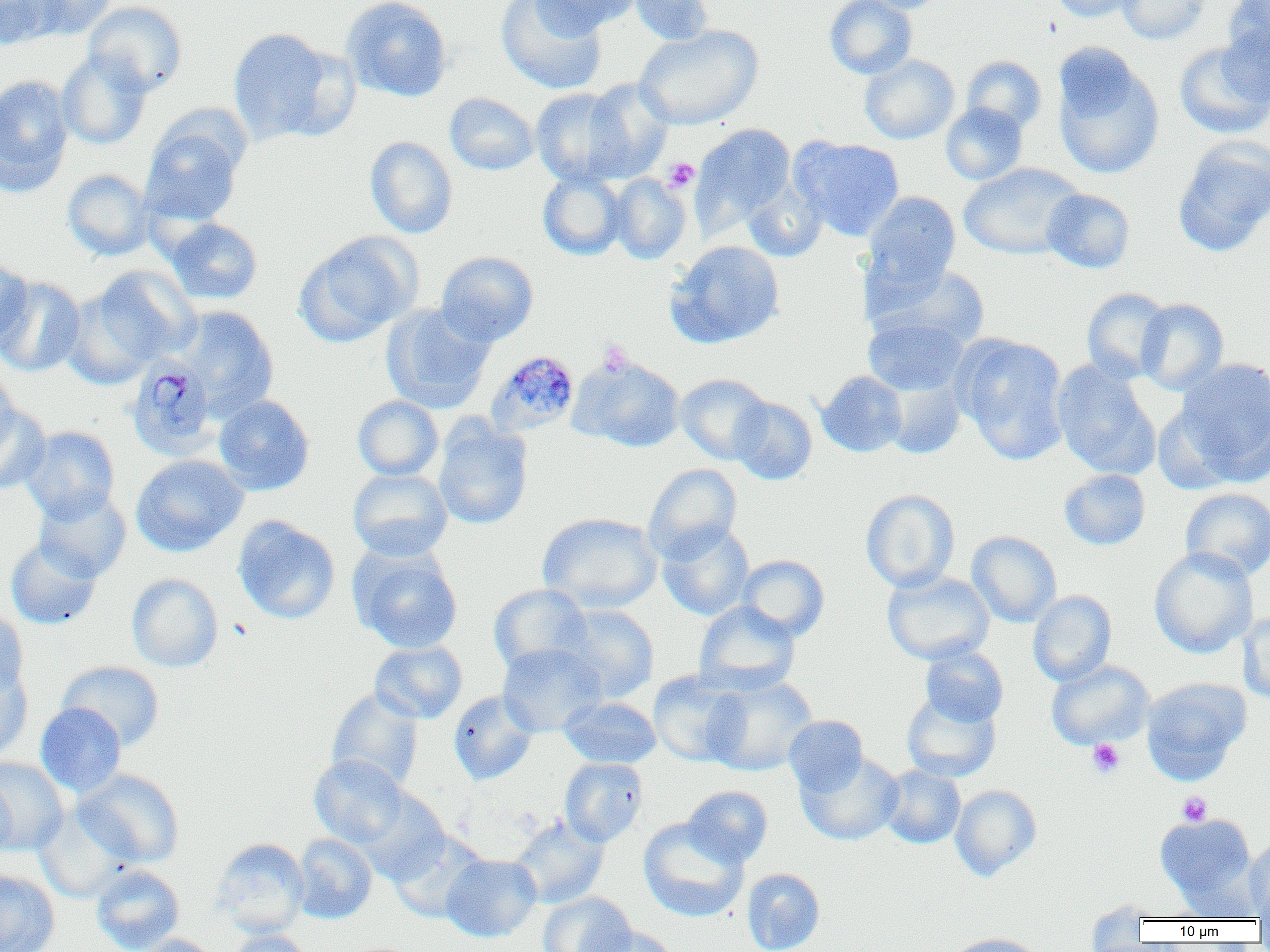
Summary:
  - Coordinate format: approximate bounding boxes as named x1/y1/x2/y2 corners in pixels
  - Uninfected red blood cell locations: (x1=0, y1=0, x2=63, y2=51), (x1=24, y1=0, x2=117, y2=39), (x1=341, y1=0, x2=452, y2=101), (x1=496, y1=0, x2=607, y2=95), (x1=528, y1=0, x2=639, y2=35), (x1=627, y1=0, x2=715, y2=45), (x1=824, y1=0, x2=917, y2=79), (x1=853, y1=0, x2=947, y2=13), (x1=1049, y1=0, x2=1142, y2=22), (x1=1115, y1=0, x2=1211, y2=44), (x1=1224, y1=0, x2=1270, y2=61), (x1=84, y1=1, x2=188, y2=96), (x1=1218, y1=18, x2=1270, y2=107), (x1=634, y1=25, x2=763, y2=130), (x1=227, y1=28, x2=347, y2=144), (x1=1174, y1=41, x2=1270, y2=139), (x1=56, y1=51, x2=152, y2=150), (x1=1051, y1=51, x2=1165, y2=180), (x1=859, y1=54, x2=959, y2=145), (x1=961, y1=56, x2=1047, y2=134), (x1=0, y1=74, x2=73, y2=195), (x1=582, y1=79, x2=674, y2=183), (x1=531, y1=88, x2=629, y2=187), (x1=444, y1=93, x2=538, y2=175), (x1=940, y1=102, x2=1028, y2=185), (x1=141, y1=120, x2=245, y2=227), (x1=691, y1=123, x2=796, y2=232), (x1=1172, y1=135, x2=1270, y2=257), (x1=365, y1=136, x2=458, y2=239), (x1=793, y1=137, x2=905, y2=240), (x1=958, y1=162, x2=1086, y2=260), (x1=62, y1=169, x2=155, y2=260), (x1=538, y1=171, x2=627, y2=259), (x1=609, y1=173, x2=691, y2=264), (x1=742, y1=179, x2=827, y2=262), (x1=1041, y1=188, x2=1135, y2=273), (x1=862, y1=191, x2=960, y2=294), (x1=164, y1=218, x2=262, y2=305), (x1=294, y1=232, x2=422, y2=347), (x1=665, y1=240, x2=785, y2=348), (x1=436, y1=251, x2=538, y2=346), (x1=0, y1=258, x2=32, y2=341), (x1=870, y1=262, x2=992, y2=350), (x1=86, y1=266, x2=200, y2=369), (x1=0, y1=276, x2=85, y2=377), (x1=62, y1=285, x2=163, y2=389), (x1=1081, y1=288, x2=1172, y2=383), (x1=1136, y1=298, x2=1229, y2=395), (x1=381, y1=303, x2=495, y2=412), (x1=174, y1=305, x2=279, y2=417), (x1=863, y1=314, x2=968, y2=396), (x1=956, y1=335, x2=1070, y2=464), (x1=570, y1=355, x2=685, y2=452), (x1=1175, y1=357, x2=1270, y2=485), (x1=1051, y1=360, x2=1160, y2=480), (x1=0, y1=366, x2=20, y2=459), (x1=817, y1=370, x2=908, y2=457), (x1=676, y1=373, x2=773, y2=464), (x1=883, y1=373, x2=966, y2=458), (x1=213, y1=394, x2=314, y2=495), (x1=352, y1=396, x2=443, y2=481), (x1=730, y1=397, x2=817, y2=485), (x1=0, y1=405, x2=50, y2=494), (x1=433, y1=418, x2=533, y2=530), (x1=20, y1=426, x2=120, y2=523), (x1=131, y1=454, x2=248, y2=557), (x1=644, y1=463, x2=742, y2=562), (x1=348, y1=469, x2=453, y2=561), (x1=1058, y1=469, x2=1150, y2=550), (x1=1180, y1=487, x2=1270, y2=581), (x1=34, y1=489, x2=132, y2=581), (x1=860, y1=489, x2=960, y2=592), (x1=537, y1=512, x2=662, y2=613), (x1=232, y1=515, x2=340, y2=624), (x1=657, y1=522, x2=755, y2=620), (x1=967, y1=531, x2=1062, y2=628), (x1=5, y1=537, x2=102, y2=630), (x1=349, y1=544, x2=463, y2=654), (x1=1149, y1=546, x2=1258, y2=658), (x1=736, y1=555, x2=829, y2=641), (x1=882, y1=570, x2=994, y2=665), (x1=126, y1=573, x2=223, y2=672), (x1=488, y1=583, x2=592, y2=674), (x1=1028, y1=590, x2=1117, y2=686), (x1=694, y1=600, x2=800, y2=694), (x1=552, y1=604, x2=660, y2=703), (x1=0, y1=607, x2=29, y2=699), (x1=1239, y1=610, x2=1270, y2=705), (x1=369, y1=640, x2=467, y2=724), (x1=497, y1=642, x2=607, y2=737), (x1=920, y1=646, x2=1008, y2=727), (x1=1046, y1=659, x2=1155, y2=750), (x1=56, y1=661, x2=165, y2=750), (x1=0, y1=662, x2=32, y2=762), (x1=648, y1=670, x2=747, y2=766), (x1=701, y1=675, x2=818, y2=776), (x1=1141, y1=677, x2=1250, y2=782), (x1=327, y1=689, x2=424, y2=791), (x1=448, y1=690, x2=538, y2=785), (x1=901, y1=690, x2=1001, y2=783), (x1=559, y1=696, x2=661, y2=768), (x1=35, y1=702, x2=126, y2=797), (x1=783, y1=715, x2=869, y2=796), (x1=796, y1=751, x2=904, y2=846), (x1=309, y1=754, x2=410, y2=848), (x1=0, y1=757, x2=70, y2=855), (x1=560, y1=758, x2=648, y2=846), (x1=878, y1=766, x2=965, y2=849), (x1=74, y1=769, x2=185, y2=867), (x1=0, y1=777, x2=17, y2=861), (x1=950, y1=784, x2=1042, y2=881), (x1=683, y1=786, x2=773, y2=868), (x1=353, y1=787, x2=451, y2=884), (x1=33, y1=804, x2=134, y2=902), (x1=1154, y1=813, x2=1259, y2=908), (x1=509, y1=815, x2=610, y2=909), (x1=638, y1=817, x2=748, y2=922), (x1=388, y1=830, x2=490, y2=924), (x1=292, y1=833, x2=377, y2=924), (x1=1244, y1=836, x2=1270, y2=919), (x1=212, y1=838, x2=310, y2=938), (x1=440, y1=854, x2=542, y2=942), (x1=91, y1=864, x2=185, y2=952), (x1=742, y1=867, x2=825, y2=952), (x1=0, y1=869, x2=60, y2=952), (x1=538, y1=892, x2=637, y2=952), (x1=1084, y1=899, x2=1167, y2=943), (x1=588, y1=925, x2=680, y2=952), (x1=226, y1=929, x2=313, y2=952), (x1=943, y1=933, x2=1047, y2=952), (x1=132, y1=934, x2=223, y2=952)
  - Plasmodium malariae-infected red blood cell locations: (x1=485, y1=350, x2=580, y2=438), (x1=131, y1=357, x2=222, y2=461)
  - Platelet locations: (x1=662, y1=157, x2=699, y2=193), (x1=597, y1=340, x2=633, y2=376), (x1=1087, y1=739, x2=1125, y2=779), (x1=1177, y1=792, x2=1211, y2=826)
  - Slide-level diagnosis: Plasmodium malariae
  - Image size: 1270×952 pixels
  - Modality: optical microscopy
  - Magnification: 1000x
  - Field of view: single
  - Preparation: thin blood film